Assess the morphology of the red blood cells.
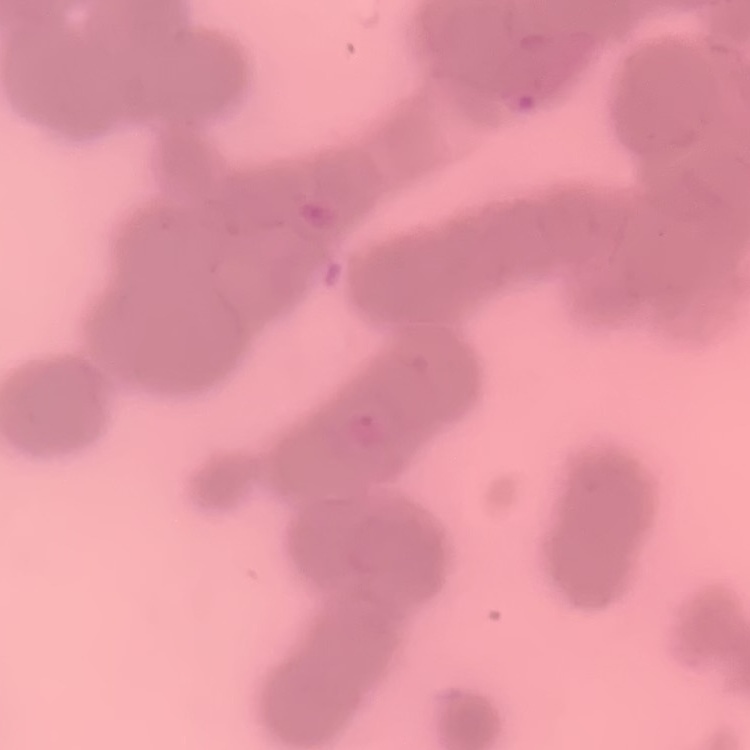
Rouleaux formation.

image_type: square crop of a larger photomicrograph
stain: Field's or Giemsa
preparation: thin blood smear